Identify the parasite.
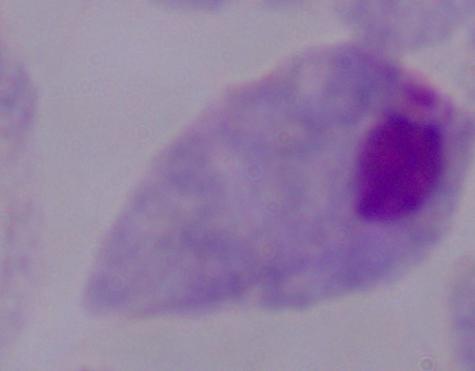

This is a trichomonad.

Micrograph. Captured at 1000x magnification.